Locate every Plasmodium vivax-infected red blood cell.
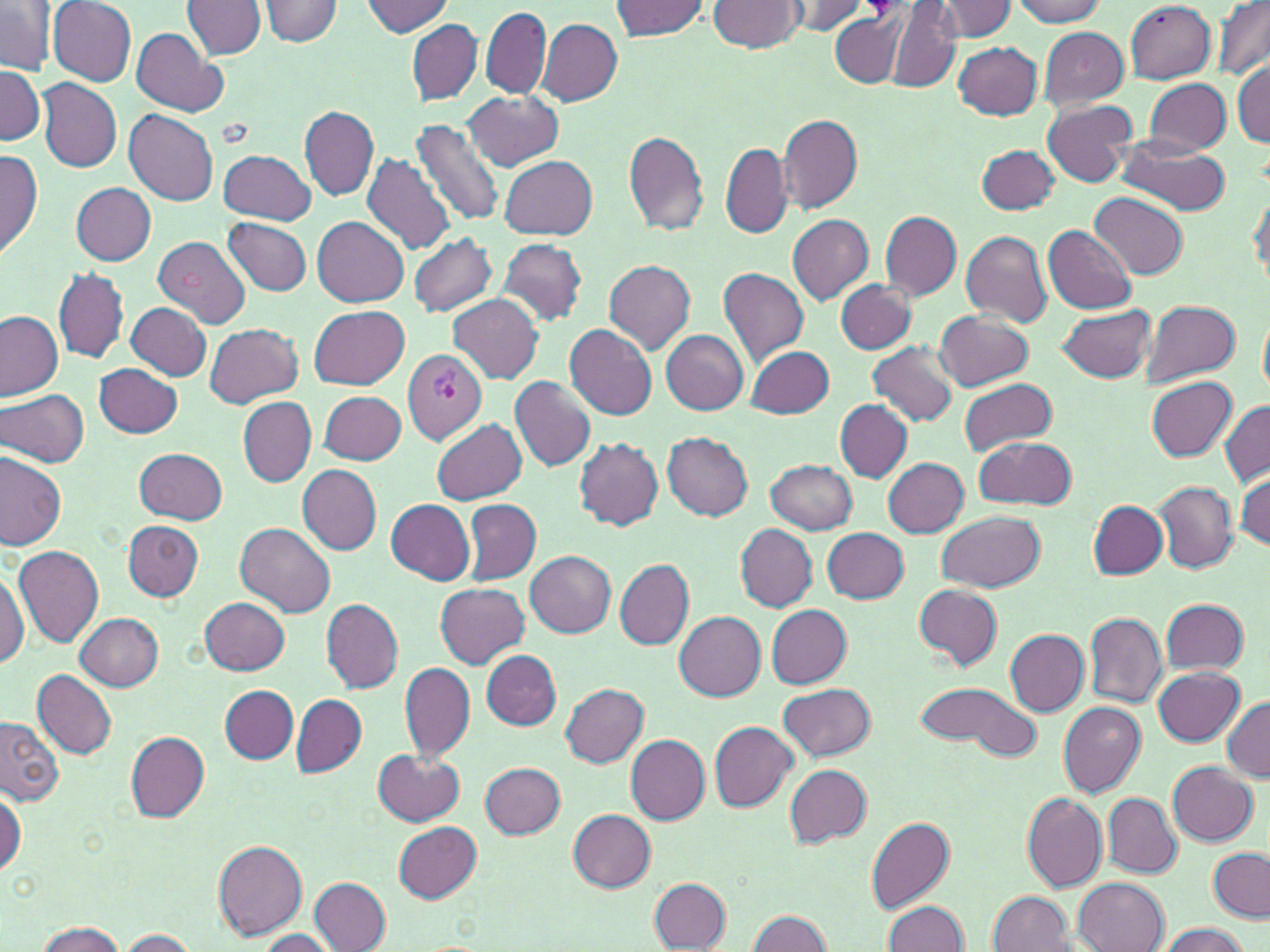
Approximate bounding boxes as (x1,y1)-(x2,y2) corner pairs in pixels.
Plasmodium vivax-infected red blood cells: (403,350)-(487,443).

Summary:
  - Uninfected red blood cell locations: (0,0)-(56,75), (183,0)-(266,60), (261,0)-(344,46), (708,0)-(805,53), (936,0)-(1019,41), (1010,0)-(1108,27), (1213,0)-(1270,81), (47,1)-(137,85), (361,1)-(454,36), (611,1)-(710,40), (786,1)-(871,36), (1126,2)-(1217,82), (888,4)-(961,92), (481,7)-(551,99), (830,13)-(904,86), (536,18)-(622,105), (407,19)-(483,104), (131,27)-(227,117), (1039,27)-(1130,110), (953,41)-(1042,120), (1231,60)-(1269,146), (0,63)-(45,146), (1143,77)-(1231,155), (38,79)-(121,173), (464,91)-(564,171), (1043,100)-(1135,186), (300,106)-(379,201), (124,109)-(218,204), (778,114)-(862,213), (409,118)-(503,228), (623,129)-(710,236), (1117,137)-(1230,215), (721,142)-(791,238), (978,145)-(1059,215), (0,150)-(43,257), (217,150)-(317,224), (362,153)-(454,254), (500,156)-(597,239), (73,183)-(156,265), (1249,187)-(1269,288), (1090,192)-(1187,279), (881,211)-(961,299), (786,215)-(874,305), (312,216)-(407,307), (223,218)-(313,297), (1044,224)-(1136,313), (307,227)-(500,310), (961,231)-(1052,326), (407,234)-(498,317), (151,235)-(250,329), (496,238)-(588,325), (601,259)-(695,355), (54,268)-(129,363), (718,268)-(809,365), (837,280)-(915,353), (449,295)-(543,384), (1141,300)-(1241,385), (125,301)-(211,381), (309,305)-(410,388), (1056,305)-(1155,384), (0,311)-(64,401), (934,312)-(1032,389), (205,323)-(303,407), (566,324)-(657,420), (661,330)-(749,416), (869,342)-(957,427), (746,346)-(834,419), (94,363)-(183,439), (509,375)-(597,472), (1147,377)-(1238,460), (959,378)-(1059,457), (0,389)-(90,468), (318,390)-(406,465), (239,396)-(315,486), (835,400)-(911,481), (1219,402)-(1270,486), (432,419)-(526,504), (662,433)-(753,520), (975,436)-(1075,510), (573,438)-(664,530), (136,447)-(225,524), (0,449)-(67,550), (882,457)-(969,538), (767,459)-(858,535), (297,465)-(382,554), (1235,472)-(1270,551), (1154,481)-(1239,573), (463,499)-(541,586), (387,500)-(475,584), (1088,500)-(1166,578), (937,511)-(1045,593), (123,520)-(203,601), (234,523)-(336,617), (735,524)-(817,611), (822,527)-(908,603), (14,545)-(104,647), (524,550)-(616,637), (616,560)-(694,649), (0,567)-(28,671), (435,582)-(529,668), (913,584)-(1003,670), (200,596)-(290,675), (320,598)-(403,693), (1161,599)-(1250,675), (766,605)-(851,687), (675,611)-(766,701), (75,612)-(164,690), (1084,612)-(1166,709), (1004,629)-(1089,715), (480,650)-(562,729), (400,662)-(473,760), (1154,667)-(1245,746), (32,669)-(117,760), (914,678)-(1041,759), (778,682)-(876,762), (560,683)-(650,767), (219,685)-(298,763), (291,694)-(367,777), (1221,695)-(1269,782), (1057,702)-(1145,797), (1,718)-(64,808), (709,721)-(797,812), (125,731)-(209,822), (626,734)-(709,824), (374,750)-(464,826), (1168,761)-(1258,846), (479,762)-(566,837), (786,763)-(872,846), (0,787)-(24,877), (1022,793)-(1107,892), (1104,793)-(1181,876), (567,809)-(656,892), (866,817)-(955,913), (393,822)-(482,902), (213,840)-(307,940), (1209,848)-(1268,920), (311,878)-(392,951), (648,878)-(732,949), (1073,878)-(1167,952), (988,891)-(1073,951), (883,901)-(971,951), (747,910)-(831,951), (35,921)-(126,952), (1155,923)-(1249,952), (118,928)-(198,950), (256,928)-(339,951)
  - Platelet locations: (862,0)-(905,19)
  - Slide-level diagnosis: Plasmodium vivax
  - Magnification: 1000x
  - Stain: May-Grünwald-Giemsa
  - Field of view: single
  - Preparation: thin blood film
  - Image size: 1270×952 pixels
  - Modality: light microscopy